Assess this cell for malaria.
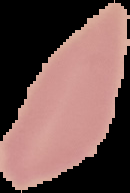
It is uninfected.

Summary:
  - Preparation: thin blood film
  - Image type: segmented cell region on a black background
  - Image size: 130×193 pixels